Classify this cell by malaria status.
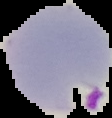
Parasitized.

Summary:
  - Preparation: thin blood smear
  - Image type: segmented cell region with the area outside set to black
  - Image size: 112×118 pixels